Classify this cell by malaria status.
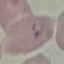
It is parasitized.

Thin blood film. Giemsa stain. Photographed with a smartphone camera at the microscope eyepiece. Automatically extracted cell patch, resized to 64 × 64 pixels.